Classify this cell by malaria status.
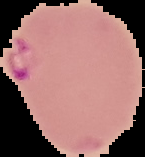
Parasitized.

Summary:
  - Image size: 145×157 pixels
  - Preparation: thin blood film
  - Image type: cell region segmented out of the field of view; surrounding area masked to black